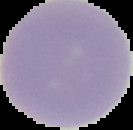

{
  "result": "no Plasmodium parasites seen",
  "image_type": "segmented cell region on a black background",
  "image_size": "133×130 pixels",
  "preparation": "thin blood smear"
}